Locate every blood parasite and identify its species.
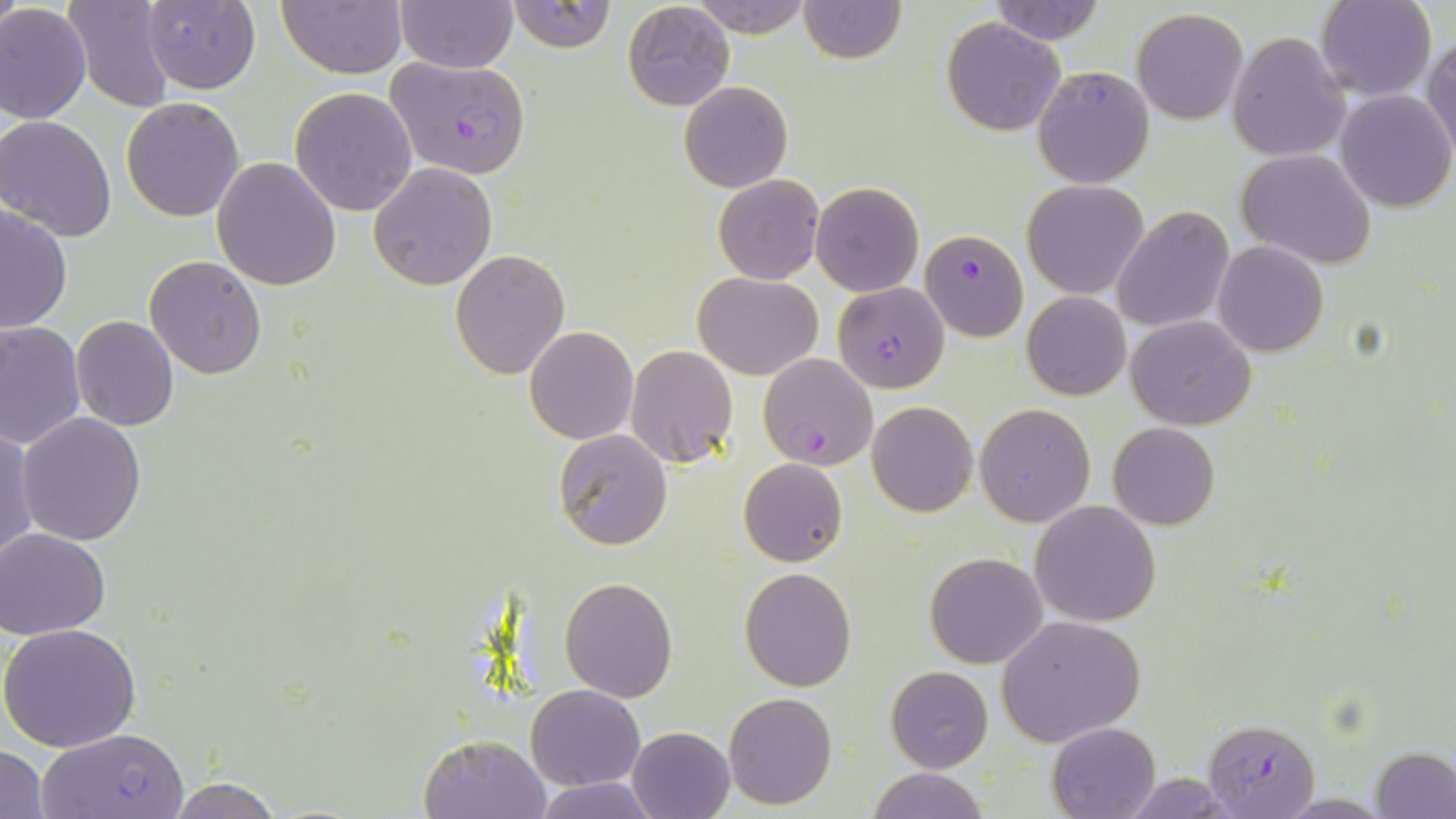

Approximate bounding boxes as (x1,y1)-(x2,y2) corner pairs in pixels.
Plasmodium falciparum-infected red blood cells: (385,53)-(531,178), (920,228)-(1029,341), (833,282)-(949,392), (758,353)-(878,470), (1202,718)-(1320,818), (37,729)-(189,817).
No Plasmodium ovale, Plasmodium malariae, Plasmodium vivax, Babesia divergens, or Trypanosoma brucei observed.

{
  "slide_level_diagnosis": "Plasmodium falciparum",
  "modality": "light microscopy",
  "magnification": "1000x",
  "image_size": "1456×819 pixels",
  "field_of_view": "single",
  "uninfected_red_blood_cell_locations": "approximate bounding boxes as (x1,y1)-(x2,y2) corner pairs in pixels: (64,0)-(179,113), (395,0)-(518,71), (505,0)-(615,53), (797,0)-(906,64), (1314,0)-(1437,102), (138,1)-(261,93), (278,1)-(406,79), (686,1)-(816,36), (987,1)-(1111,47), (622,2)-(735,112), (0,3)-(91,124), (1132,8)-(1249,125), (942,17)-(1067,136), (1226,32)-(1351,162), (1424,36)-(1456,155), (1033,65)-(1154,188), (679,81)-(793,193), (290,87)-(417,215), (1334,89)-(1455,212), (121,97)-(244,221), (0,115)-(118,242), (1236,149)-(1378,268), (211,156)-(342,290), (368,162)-(496,290), (713,175)-(823,285), (1022,180)-(1149,298), (811,182)-(923,296), (0,203)-(72,333), (1112,206)-(1234,334), (1213,240)-(1328,357), (450,248)-(569,379), (144,256)-(268,378), (693,270)-(822,380), (1022,291)-(1131,401), (70,315)-(179,430), (1126,315)-(1257,430), (0,322)-(85,447), (524,326)-(638,444), (625,344)-(738,468), (866,401)-(977,517), (974,403)-(1096,526), (15,411)-(148,546), (1107,423)-(1220,530), (1,425)-(37,564), (553,431)-(673,550), (739,457)-(848,567), (1030,502)-(1162,626), (1,528)-(113,639), (924,552)-(1048,669), (738,566)-(857,692), (559,576)-(677,702), (996,615)-(1146,746), (1,624)-(141,753), (885,665)-(993,773), (526,684)-(645,790), (722,692)-(837,810), (1046,722)-(1162,818), (626,726)-(734,819), (418,733)-(551,818), (1,744)-(50,818), (1372,746)-(1456,817), (866,766)-(987,819), (1120,772)-(1241,816), (163,776)-(289,819), (534,777)-(659,818), (1273,793)-(1391,817)",
  "preparation": "thin blood film",
  "stain": "May-Grünwald-Giemsa"
}